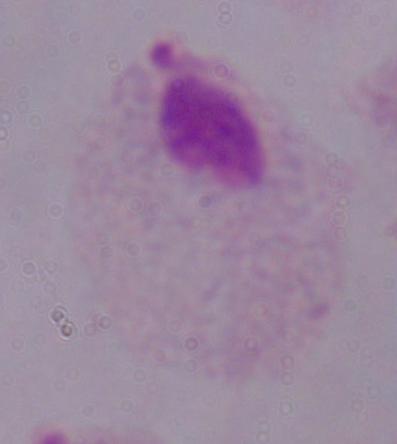
A trichomonad is shown. Captured at 1000x magnification. Photomicrograph.